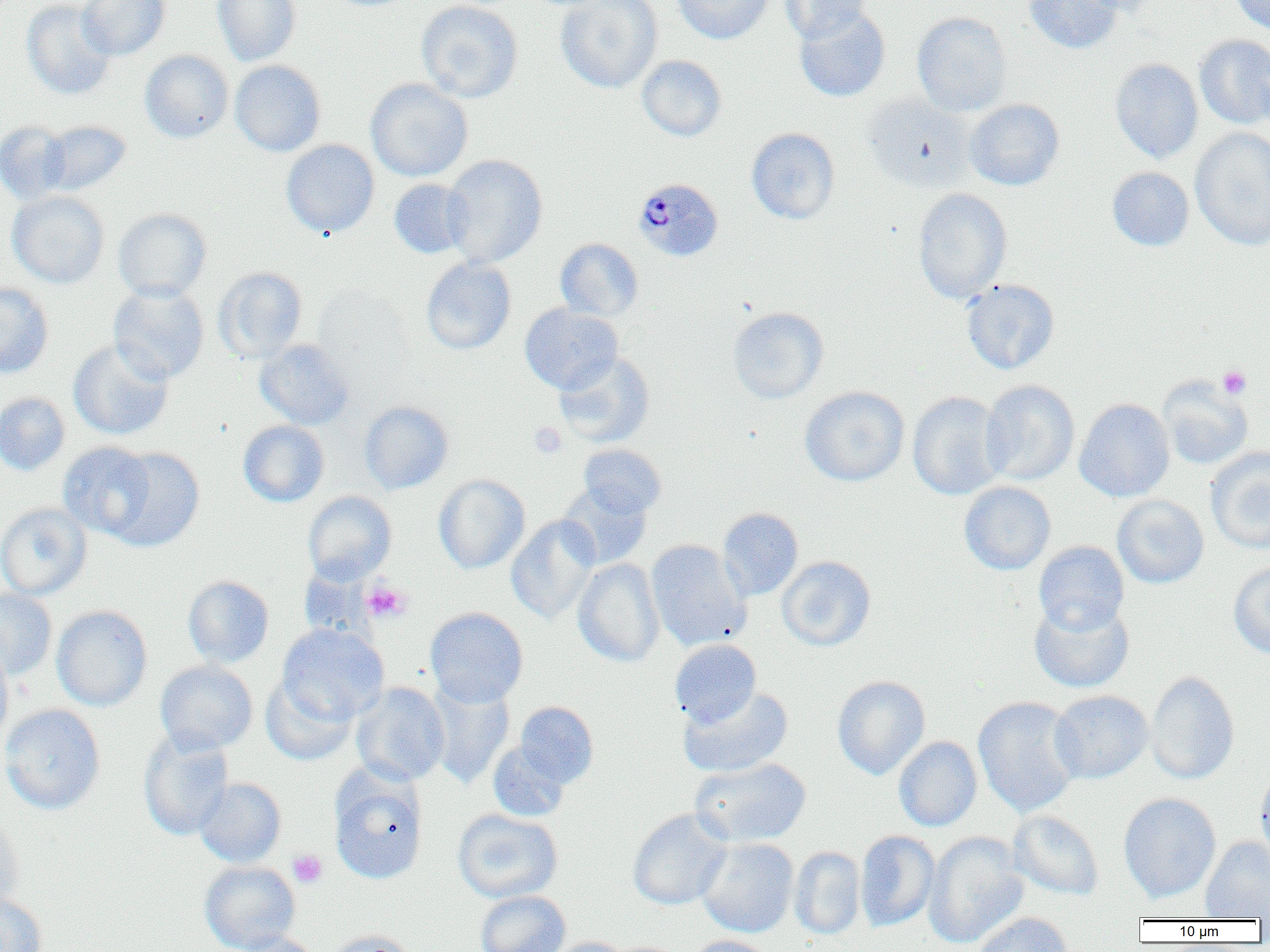 Approximate bounding boxes as [x1, y1, x2, y2] in pixels. Plasmodium malariae-infected red blood cell locations: [632, 177, 724, 262]. Uninfected red blood cell locations: [21, 0, 116, 100], [77, 0, 170, 60], [212, 0, 300, 65], [416, 0, 523, 103], [554, 0, 663, 93], [672, 0, 775, 44], [780, 0, 870, 44], [1024, 0, 1124, 54], [1077, 0, 1170, 15], [1231, 0, 1270, 34], [793, 5, 891, 102], [911, 11, 1012, 116], [1194, 34, 1270, 129], [140, 50, 234, 143], [636, 55, 727, 141], [1110, 58, 1203, 162], [230, 60, 326, 156], [365, 78, 473, 182], [861, 93, 976, 192], [964, 98, 1064, 190], [40, 120, 131, 196], [0, 121, 72, 204], [745, 127, 840, 224], [1190, 128, 1270, 250], [281, 139, 380, 238], [442, 154, 548, 268], [1107, 167, 1194, 251], [389, 179, 473, 259], [912, 188, 1012, 304], [7, 191, 110, 288], [113, 208, 212, 302], [555, 238, 644, 321], [420, 256, 516, 354], [213, 266, 307, 363], [961, 278, 1060, 375], [0, 282, 53, 378], [108, 284, 209, 383], [519, 303, 623, 393], [727, 306, 829, 404], [68, 338, 174, 440], [255, 339, 355, 430], [553, 353, 654, 447], [1158, 376, 1253, 469], [980, 380, 1080, 486], [800, 385, 910, 487], [907, 391, 1007, 500], [0, 392, 70, 476], [1074, 398, 1174, 502], [359, 401, 454, 494], [238, 420, 330, 507], [58, 442, 156, 539], [578, 443, 667, 518], [106, 447, 205, 552], [1205, 447, 1270, 553], [433, 473, 530, 574], [959, 481, 1056, 575], [558, 482, 652, 570], [302, 491, 396, 584], [1111, 495, 1209, 588], [0, 502, 92, 600], [717, 507, 803, 600], [505, 515, 600, 624], [646, 540, 750, 651], [1034, 540, 1129, 635], [777, 555, 875, 652], [573, 558, 665, 667], [1228, 562, 1270, 658], [183, 575, 274, 668], [0, 588, 57, 680], [1029, 597, 1134, 693], [51, 605, 153, 711], [425, 607, 528, 707], [277, 624, 389, 724], [670, 639, 761, 727], [0, 643, 13, 748], [155, 660, 258, 754], [1145, 670, 1239, 785], [260, 674, 358, 765], [832, 675, 931, 779], [425, 679, 515, 788], [351, 682, 450, 786], [678, 686, 794, 777], [1049, 690, 1153, 783], [973, 696, 1082, 817], [515, 701, 598, 787], [0, 704, 105, 814], [139, 728, 234, 840], [893, 736, 982, 831], [488, 740, 571, 821], [690, 757, 812, 847], [1255, 765, 1270, 871], [329, 769, 429, 884], [195, 777, 286, 868], [1119, 793, 1221, 903], [627, 808, 732, 910], [453, 809, 562, 902], [1008, 810, 1104, 900], [0, 817, 24, 913], [855, 830, 940, 932], [924, 831, 1030, 948], [1200, 836, 1270, 919], [696, 838, 798, 937], [789, 846, 866, 940], [199, 861, 300, 952], [475, 890, 571, 952], [0, 894, 48, 952], [970, 912, 1074, 952], [323, 930, 418, 952], [226, 932, 321, 952], [684, 935, 776, 952], [542, 936, 634, 952]. Platelet locations: [1218, 365, 1252, 399], [528, 422, 567, 458], [362, 581, 411, 623], [288, 849, 328, 888]. Slide-level diagnosis: Plasmodium malariae. Optical microscopy. One field of a larger specimen. Image is 1270×952 pixels. Thin blood smear. 1000x magnification.